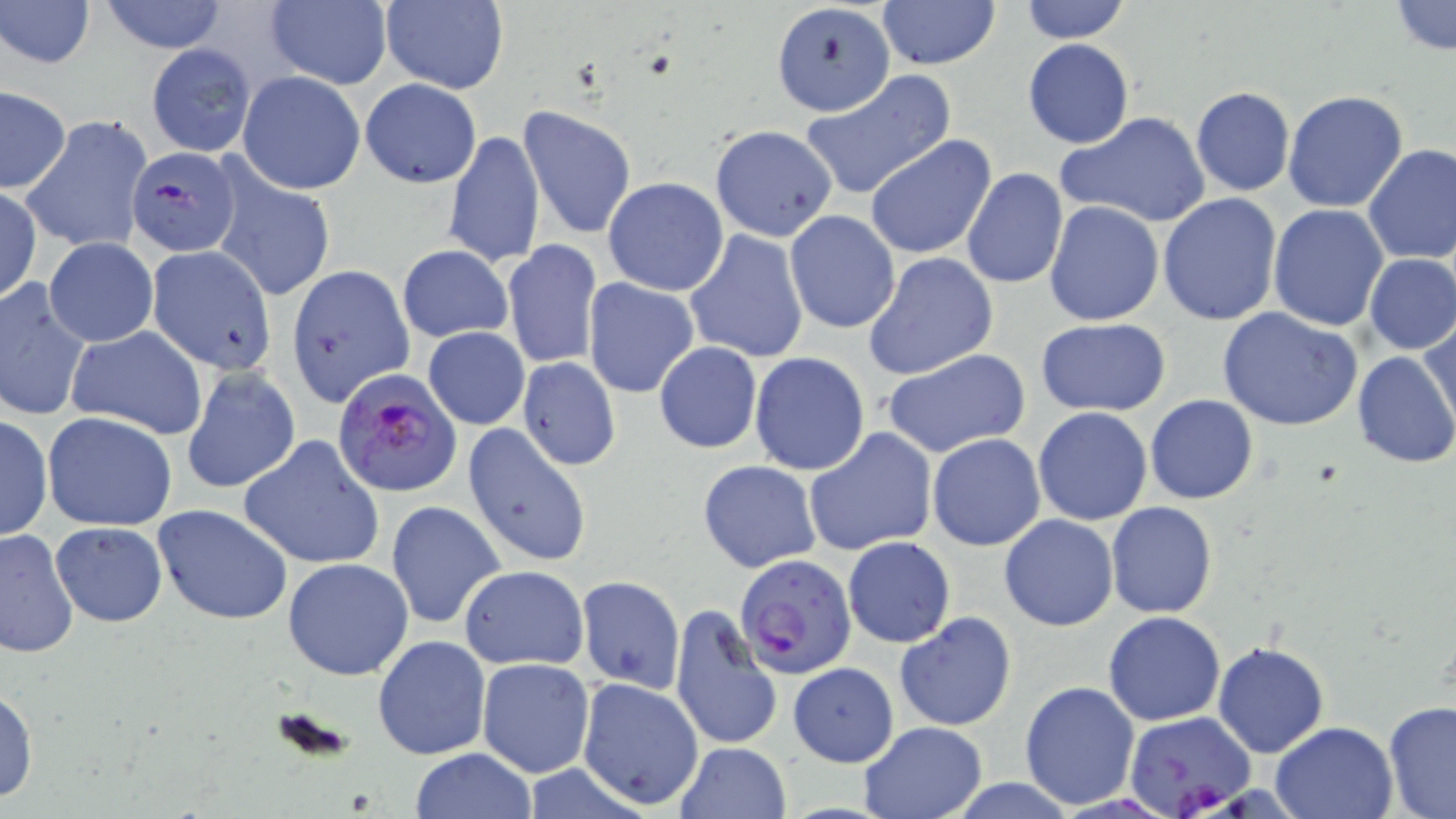
Summary:
  - Coordinate format: approximate bounding boxes as named x1/y1/x2/y2 corners in pixels
  - Plasmodium falciparum-infected red blood cell locations: (x1=127, y1=146, x2=240, y2=256), (x1=332, y1=369, x2=461, y2=498), (x1=731, y1=553, x2=855, y2=679), (x1=1124, y1=711, x2=1254, y2=816)
  - Uninfected red blood cell locations: (x1=1, y1=0, x2=95, y2=71), (x1=98, y1=0, x2=230, y2=53), (x1=378, y1=0, x2=509, y2=94), (x1=878, y1=0, x2=1000, y2=71), (x1=1017, y1=0, x2=1133, y2=43), (x1=263, y1=1, x2=392, y2=90), (x1=771, y1=1, x2=895, y2=116), (x1=1389, y1=1, x2=1454, y2=55), (x1=1022, y1=39, x2=1134, y2=149), (x1=146, y1=44, x2=255, y2=157), (x1=800, y1=70, x2=957, y2=200), (x1=237, y1=71, x2=365, y2=195), (x1=359, y1=78, x2=482, y2=189), (x1=1190, y1=86, x2=1295, y2=196), (x1=0, y1=87, x2=70, y2=193), (x1=1281, y1=90, x2=1409, y2=213), (x1=518, y1=106, x2=636, y2=240), (x1=1056, y1=111, x2=1212, y2=229), (x1=22, y1=117, x2=151, y2=254), (x1=709, y1=124, x2=837, y2=241), (x1=443, y1=129, x2=545, y2=271), (x1=865, y1=135, x2=998, y2=259), (x1=1363, y1=143, x2=1456, y2=265), (x1=212, y1=166, x2=336, y2=302), (x1=961, y1=168, x2=1068, y2=290), (x1=603, y1=176, x2=728, y2=296), (x1=1, y1=188, x2=42, y2=305), (x1=1158, y1=192, x2=1284, y2=326), (x1=1044, y1=200, x2=1163, y2=326), (x1=1269, y1=204, x2=1388, y2=330), (x1=785, y1=210, x2=902, y2=334), (x1=683, y1=229, x2=809, y2=364), (x1=44, y1=238, x2=158, y2=349), (x1=502, y1=240, x2=602, y2=368), (x1=397, y1=245, x2=513, y2=342), (x1=147, y1=246, x2=276, y2=374), (x1=863, y1=252, x2=998, y2=381), (x1=1363, y1=253, x2=1456, y2=355), (x1=288, y1=265, x2=416, y2=407), (x1=0, y1=277, x2=93, y2=423), (x1=583, y1=277, x2=700, y2=397), (x1=1216, y1=306, x2=1362, y2=431), (x1=1421, y1=317, x2=1456, y2=435), (x1=1035, y1=319, x2=1172, y2=416), (x1=65, y1=326, x2=208, y2=441), (x1=423, y1=327, x2=529, y2=430), (x1=653, y1=341, x2=763, y2=453), (x1=882, y1=348, x2=1031, y2=460), (x1=1351, y1=349, x2=1456, y2=468), (x1=750, y1=352, x2=870, y2=476), (x1=518, y1=358, x2=620, y2=469), (x1=182, y1=368, x2=300, y2=494), (x1=1145, y1=395, x2=1258, y2=505), (x1=1033, y1=406, x2=1152, y2=526), (x1=42, y1=410, x2=179, y2=531), (x1=0, y1=414, x2=52, y2=541), (x1=463, y1=422, x2=592, y2=569), (x1=804, y1=428, x2=937, y2=556), (x1=928, y1=434, x2=1046, y2=552), (x1=240, y1=436, x2=385, y2=571), (x1=698, y1=460, x2=821, y2=573), (x1=385, y1=500, x2=506, y2=630), (x1=1106, y1=501, x2=1218, y2=618), (x1=154, y1=504, x2=295, y2=625), (x1=999, y1=514, x2=1119, y2=632), (x1=51, y1=522, x2=167, y2=627), (x1=0, y1=526, x2=78, y2=658), (x1=843, y1=537, x2=956, y2=647), (x1=283, y1=557, x2=414, y2=680), (x1=459, y1=565, x2=589, y2=670), (x1=577, y1=576, x2=685, y2=693), (x1=588, y1=583, x2=756, y2=718), (x1=669, y1=604, x2=781, y2=754), (x1=894, y1=611, x2=1017, y2=730), (x1=1103, y1=611, x2=1226, y2=726), (x1=372, y1=635, x2=491, y2=758), (x1=1211, y1=642, x2=1329, y2=757), (x1=478, y1=658, x2=595, y2=776), (x1=788, y1=662, x2=899, y2=767), (x1=576, y1=678, x2=705, y2=811), (x1=1018, y1=681, x2=1141, y2=809), (x1=1, y1=686, x2=38, y2=804), (x1=1382, y1=701, x2=1456, y2=818), (x1=858, y1=720, x2=988, y2=818), (x1=1271, y1=720, x2=1398, y2=818), (x1=673, y1=742, x2=793, y2=819), (x1=409, y1=749, x2=538, y2=818)
  - Slide-level diagnosis: Plasmodium falciparum
  - Preparation: thin blood film
  - Field of view: single
  - Modality: light microscopy
  - Stain: May-Grünwald-Giemsa
  - Image size: 1456×819 pixels
  - Magnification: 1000x